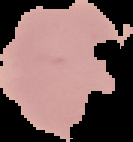

Summary:
  - Malaria status: uninfected
  - Image type: segmented cell region with the area outside set to black
  - Preparation: thin blood smear
  - Image size: 133×142 pixels